Classify this cell by malaria status.
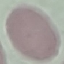
It is uninfected.

Summary:
  - Image type: cell patch, automatically extracted from a larger field of view and resized to 64 × 64 pixels
  - Capture: smartphone through the microscope eyepiece
  - Stain: Giemsa
  - Preparation: thin blood film